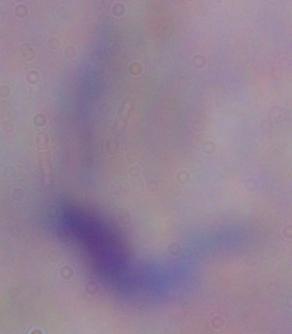
Summary:
  - Identification: trypanosome
  - Modality: photomicrograph
  - Magnification: 1000x